Assess this cell for malaria.
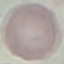

Uninfected.

Giemsa stain. Automatically extracted cell patch, resized to 64 × 64 pixels. Photographed with a smartphone camera at the microscope eyepiece. Thin smear of blood.